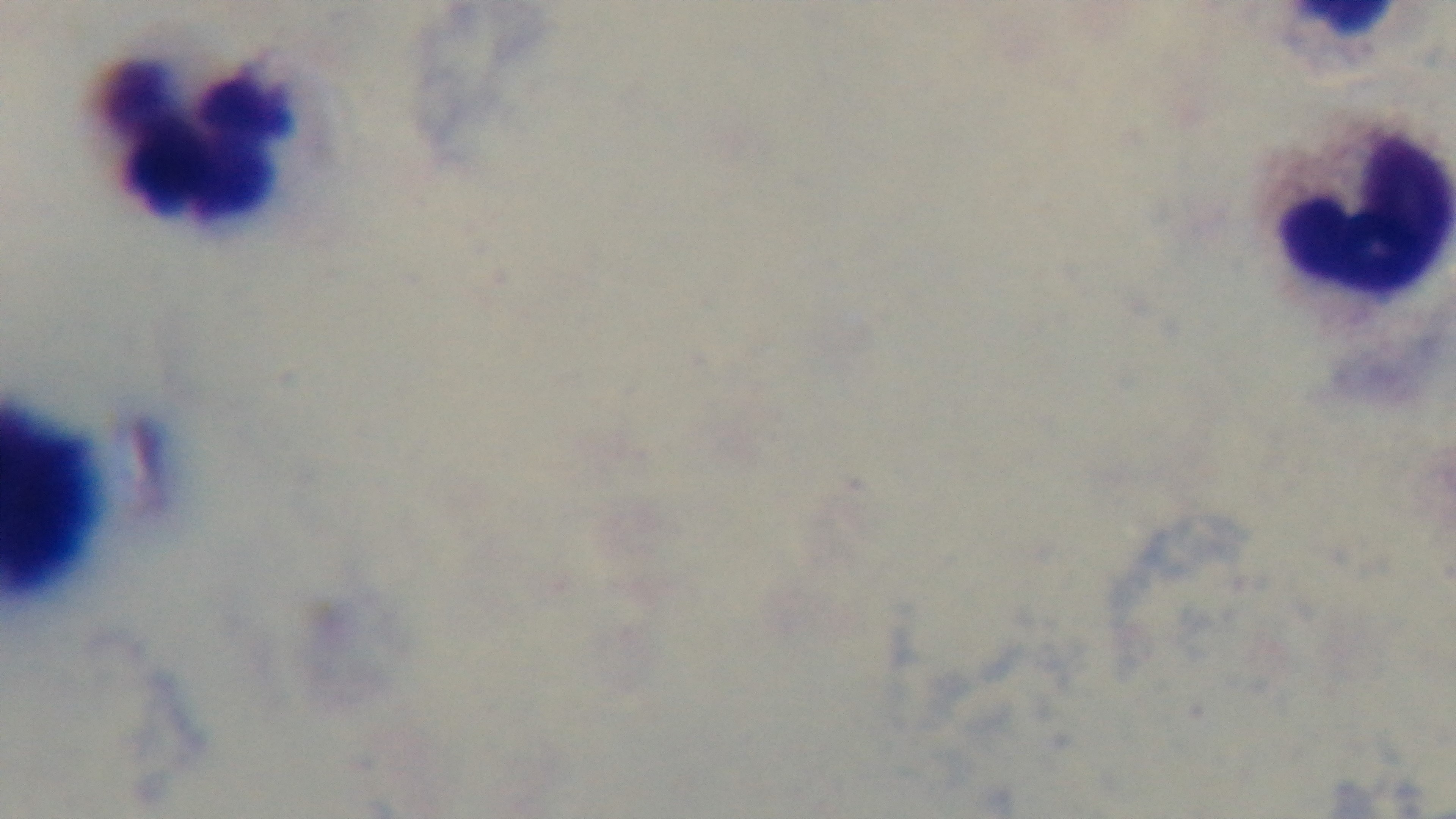 Preparation: thick blood film. One field from the slide. Mounted 4K digital camera. Giemsa-stained. Malaria status: negative. 100x oil-immersion objective. Photomicrograph.